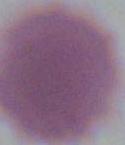

magnification = 1000x
identification = red blood cell
modality = photomicrograph